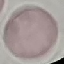
Malaria status: uninfected. Giemsa stain. Thin blood smear. Cell patch, automatically extracted from a larger field of view and resized to 64 × 64 pixels. Photographed with a smartphone camera at the microscope eyepiece.